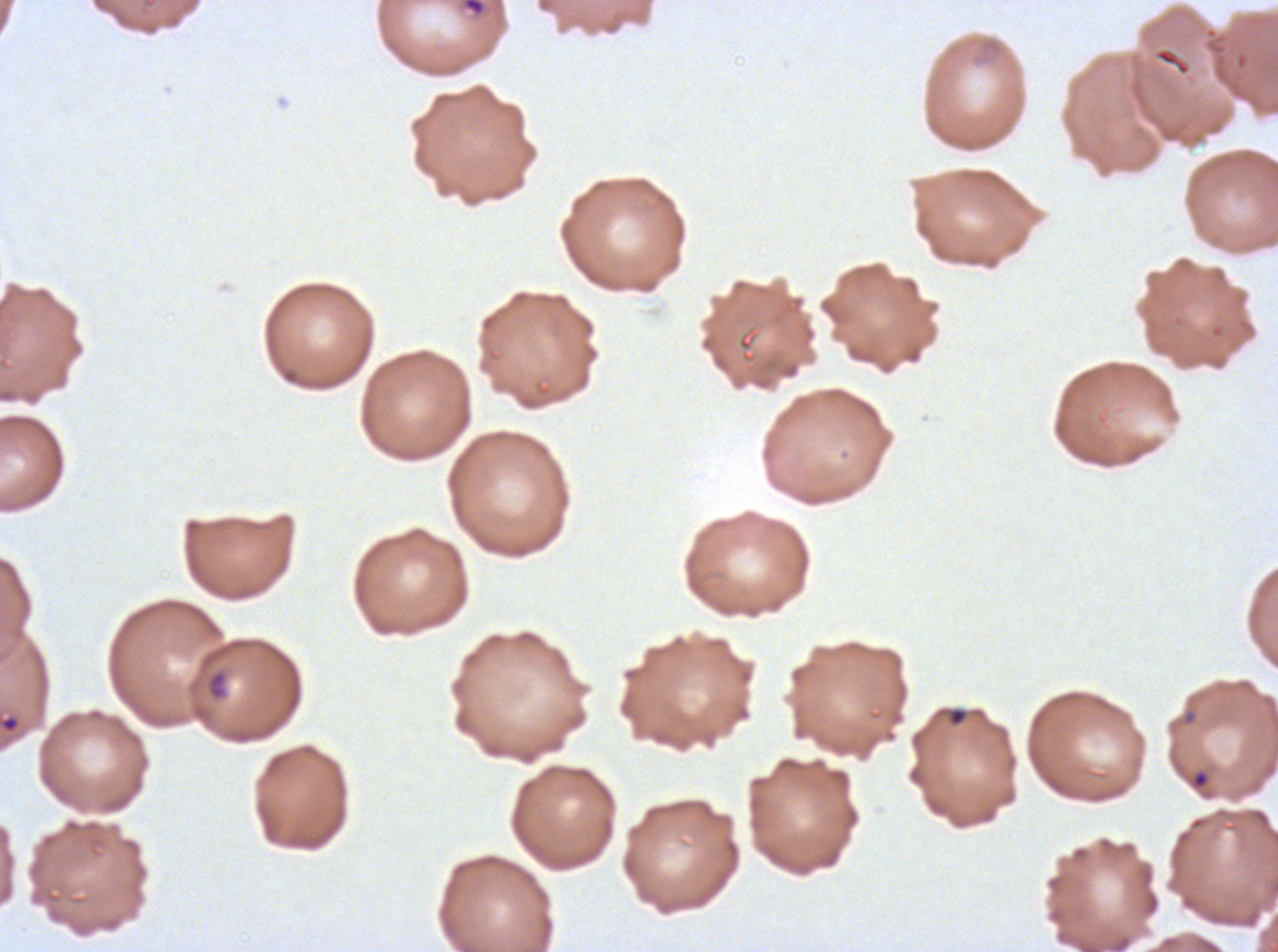

notation = approximate bounding boxes as [x1, y1, x2, y2] in pixels
ring locations = [462, 0, 485, 16], [206, 669, 227, 700], [947, 707, 967, 726], [1192, 771, 1209, 788]
stain = Giemsa
image size = 1278×952 pixels
field of view = one sub-image of a larger composite
preparation = thin blood film
specimen = P. falciparum from a patient in The Gambia, cultured ex vivo for 24 to 48 hours